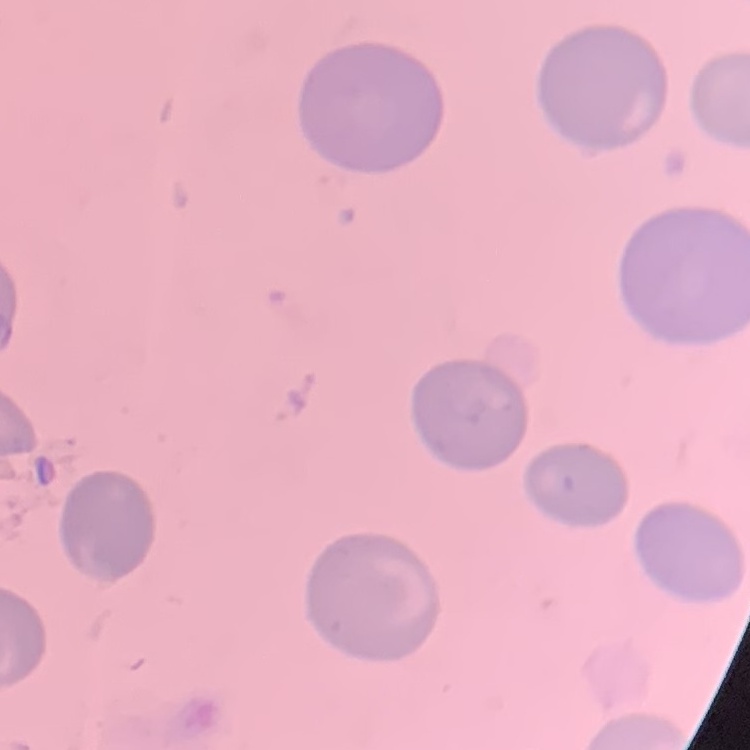

Summary:
  - Erythrocyte morphology: no rouleaux formation
  - Image type: one tile cut from a larger photomicrograph
  - Stain: Field's or Giemsa
  - Preparation: thin peripheral smear